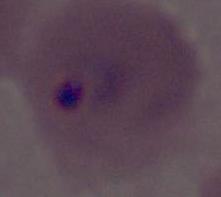

Summary:
  - Identification: Plasmodium
  - Magnification: 400x or 1000x
  - Modality: photomicrograph